Classify this cell by malaria status.
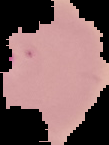

It is parasitized.

Cell region segmented out of the field of view; the surrounding area is masked to black. Image is 109×145 pixels. From a thin blood film.